Identify the preparation type.
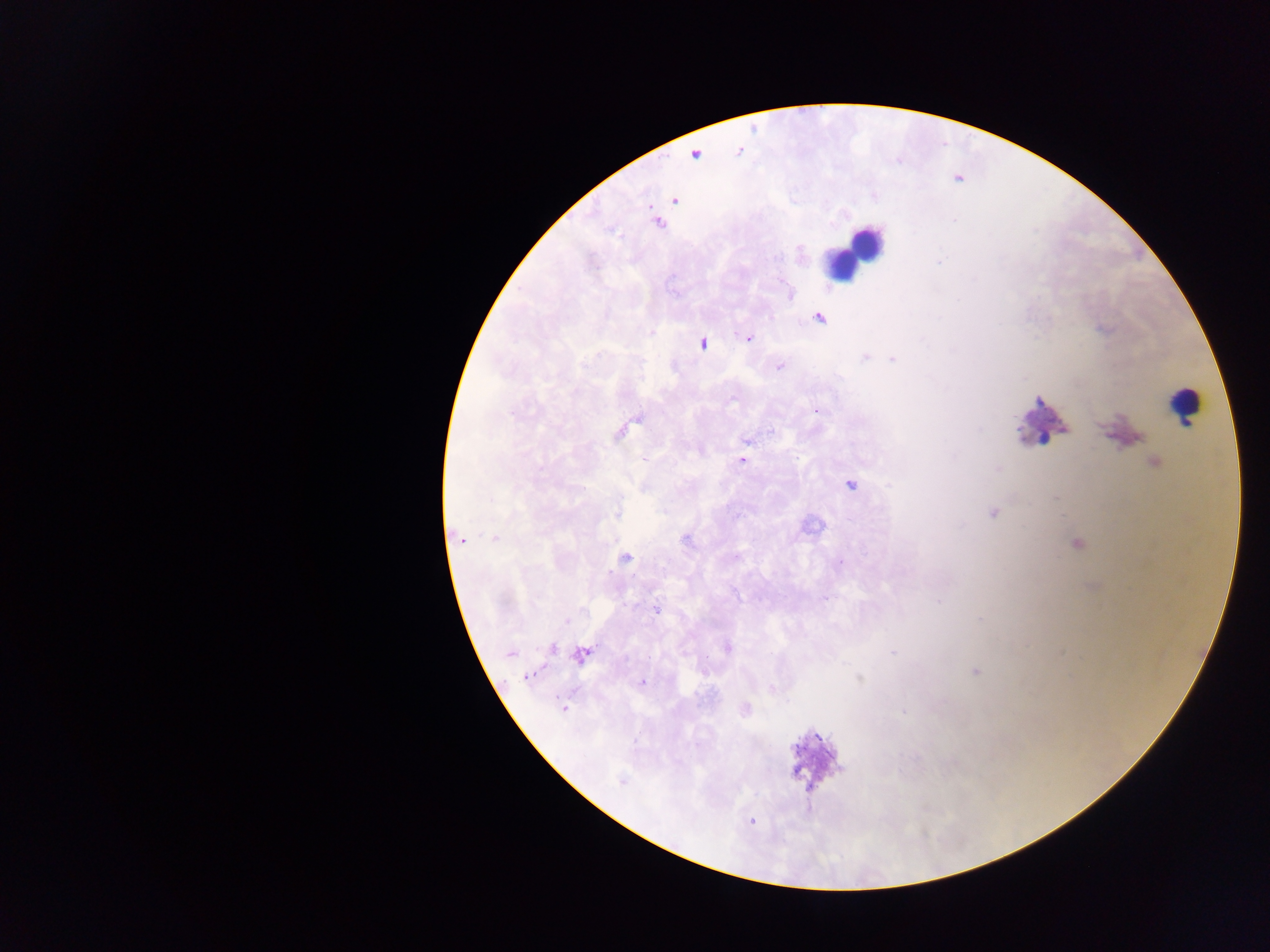
Thick blood film.

Approximate centers as {x, y} in pixels.
Summary:
  - Leukocyte locations: {855, 250}, {1181, 405}, {1041, 415}
  - Plasmodium parasite locations: {675, 200}, {820, 317}, {748, 338}, {702, 342}, {865, 358}, {892, 359}, {780, 367}, {816, 411}, {619, 433}, {644, 460}, {742, 460}, {998, 469}, {850, 485}, {993, 513}, {495, 539}, {460, 540}, {685, 540}, {736, 557}, {625, 558}, {656, 608}, {566, 622}, {551, 647}, {727, 648}, {892, 652}, {510, 654}, {582, 655}, {649, 657}, {975, 672}, {527, 676}, {859, 677}, {642, 682}, {564, 708}, {621, 780}, {752, 821}
  - Capture: mobile-phone photograph through a microscope
  - Image size: 1270×952 pixels
  - Country: Ghana
  - Field of view: single